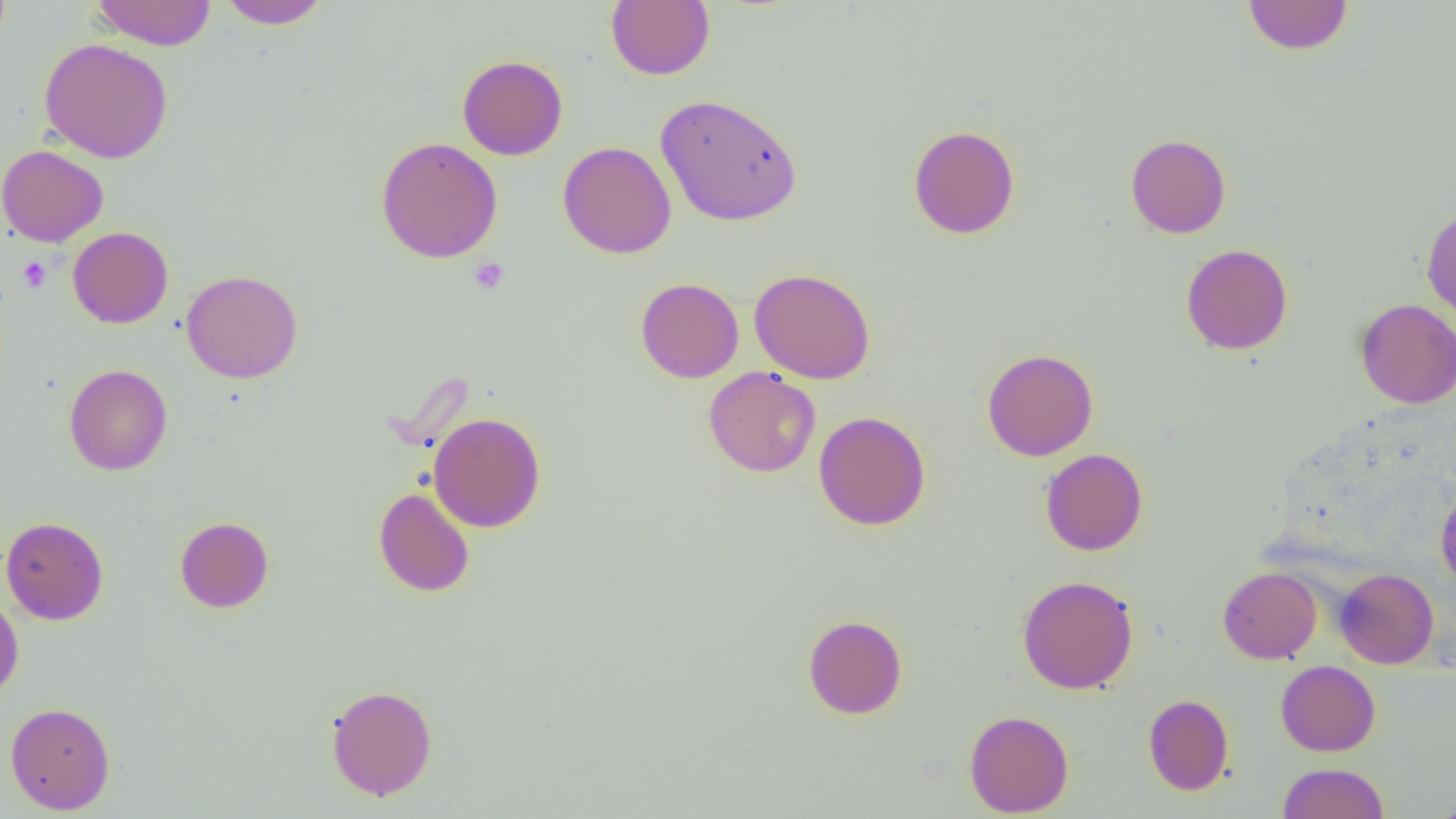
{
  "slide_level_diagnosis": "negative for blood parasites",
  "platelet_locations": "approximate bounding boxes as named x1/y1/x2/y2 corners in pixels: (x1=17, y1=256, x2=52, y2=293), (x1=468, y1=258, x2=510, y2=295)",
  "modality": "optical microscopy",
  "image_size": "1456×819 pixels",
  "field_of_view": "single",
  "magnification": "1000x",
  "uninfected_red_blood_cell_locations": "approximate bounding boxes as named x1/y1/x2/y2 corners in pixels: (x1=90, y1=0, x2=217, y2=50), (x1=1242, y1=0, x2=1353, y2=55), (x1=217, y1=1, x2=332, y2=30), (x1=605, y1=1, x2=715, y2=80), (x1=39, y1=38, x2=173, y2=163), (x1=457, y1=55, x2=568, y2=160), (x1=655, y1=93, x2=802, y2=226), (x1=908, y1=124, x2=1020, y2=239), (x1=1125, y1=134, x2=1231, y2=238), (x1=375, y1=137, x2=503, y2=263), (x1=558, y1=141, x2=676, y2=259), (x1=0, y1=144, x2=108, y2=247), (x1=1421, y1=205, x2=1456, y2=327), (x1=67, y1=226, x2=173, y2=328), (x1=1180, y1=243, x2=1293, y2=355), (x1=749, y1=268, x2=876, y2=384), (x1=181, y1=269, x2=303, y2=383), (x1=635, y1=277, x2=744, y2=383), (x1=1355, y1=298, x2=1456, y2=408), (x1=981, y1=348, x2=1098, y2=461), (x1=63, y1=364, x2=173, y2=476), (x1=703, y1=367, x2=820, y2=478), (x1=814, y1=410, x2=931, y2=531), (x1=428, y1=412, x2=546, y2=532), (x1=1040, y1=448, x2=1148, y2=556), (x1=1436, y1=485, x2=1456, y2=590), (x1=373, y1=487, x2=475, y2=597), (x1=0, y1=516, x2=109, y2=625), (x1=174, y1=516, x2=274, y2=613), (x1=1217, y1=566, x2=1321, y2=664), (x1=1335, y1=568, x2=1438, y2=669), (x1=1017, y1=575, x2=1138, y2=694), (x1=0, y1=593, x2=24, y2=705), (x1=802, y1=614, x2=907, y2=719), (x1=1276, y1=660, x2=1380, y2=756), (x1=325, y1=684, x2=438, y2=800), (x1=1143, y1=694, x2=1234, y2=795), (x1=5, y1=702, x2=115, y2=814), (x1=964, y1=709, x2=1074, y2=817), (x1=1277, y1=762, x2=1390, y2=819), (x1=1429, y1=798, x2=1456, y2=818)",
  "preparation": "thin blood smear"
}